Name the parasite shown.
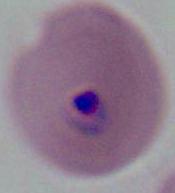

This is Plasmodium.

Summary:
  - Magnification: 400x or 1000x
  - Modality: micrograph